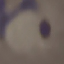

Malaria status: parasitized. Giemsa stain. Cell patch, automatically extracted from a larger field of view and resized to 64 × 64 pixels. Acquired by smartphone through the microscope eyepiece. Thin smear of blood.